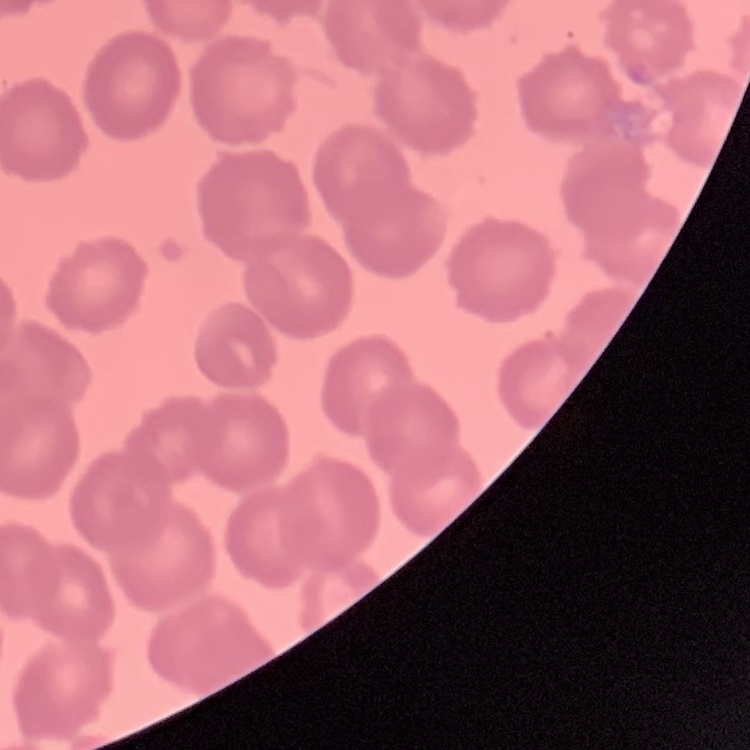
erythrocyte morphology = no rouleaux formation
image type = one tile cut from a larger photomicrograph
stain = Field's or Giemsa
preparation = thin blood smear